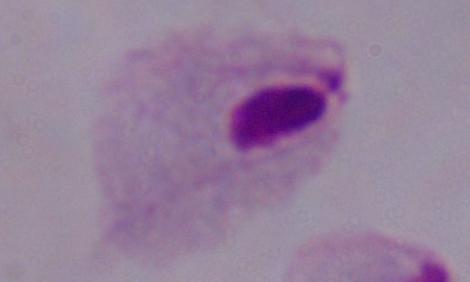
Summary:
  - Magnification: 1000x
  - Modality: photomicrograph
  - Identification: trichomonad